Assess this cell for malaria.
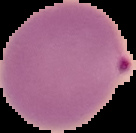
It is parasitized.

image type = segmented cell region with the area outside set to black
preparation = thin blood film
image size = 136×133 pixels